Locate every Plasmodium falciparum parasite and give its life-cycle stage, and locate every leukocyte and any debris.
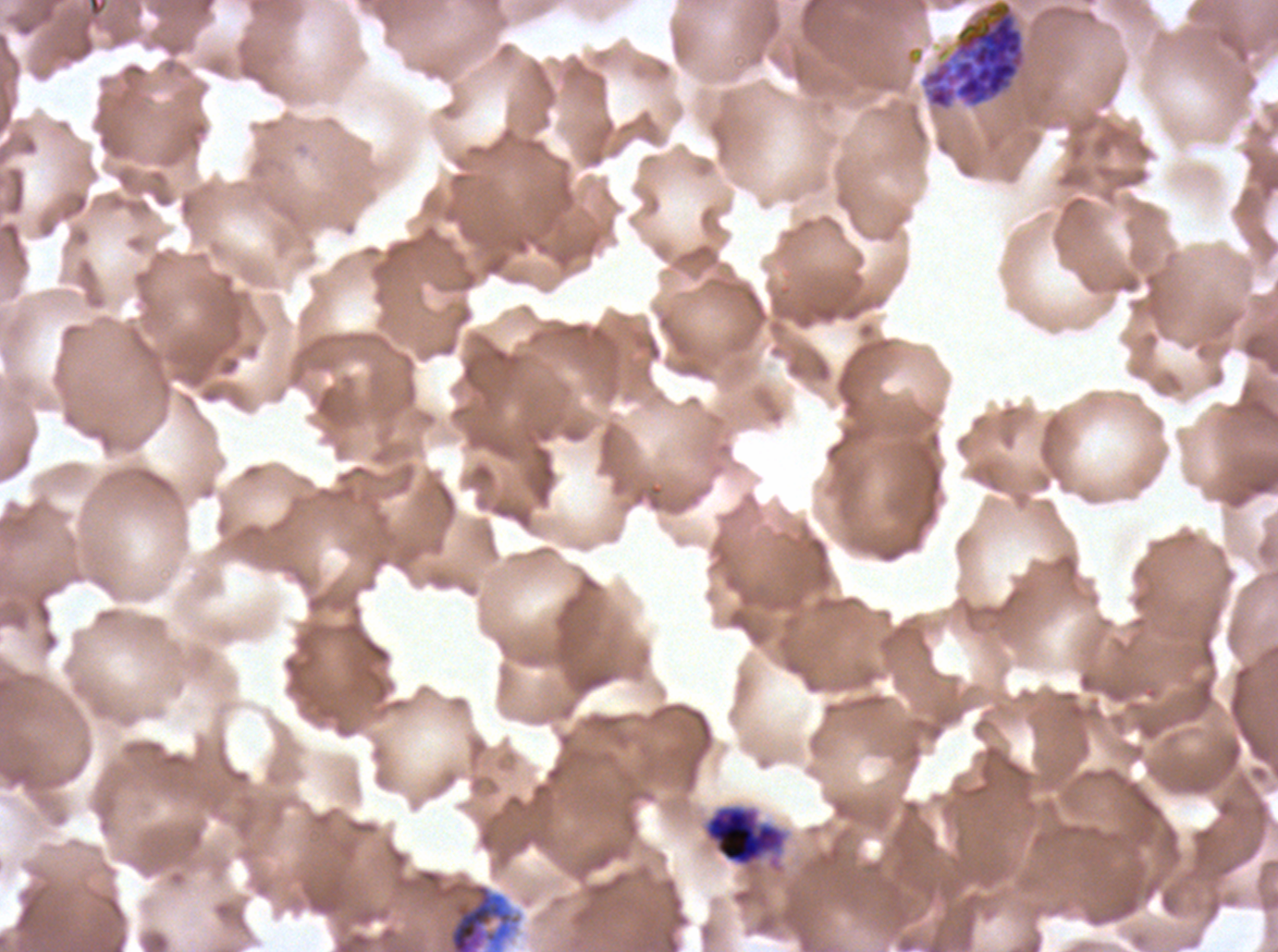

Approximate bounding boxes as (x1, y1, x2, y2) in pixels.
Early schizonts: (920, 0, 1026, 111), (702, 803, 788, 871), (448, 883, 513, 951).
No rings, late-ring/early-trophozoite forms, mid trophozoites, late trophozoites, late schizonts, segmenters, gametocytes, leukocytes, or debris observed.

specimen: Plasmodium falciparum cultured ex vivo for 24 to 48 hours, from a patient in The Gambia
image_size: 1278×952 pixels
field_of_view: sub-image separated from a larger composite
preparation: thin blood film
stain: Giemsa